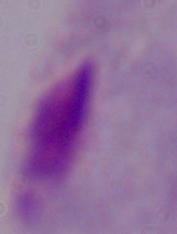
modality: micrograph
identification: trichomonad
magnification: 1000x